Outline each Plasmodium malariae-infected red blood cell.
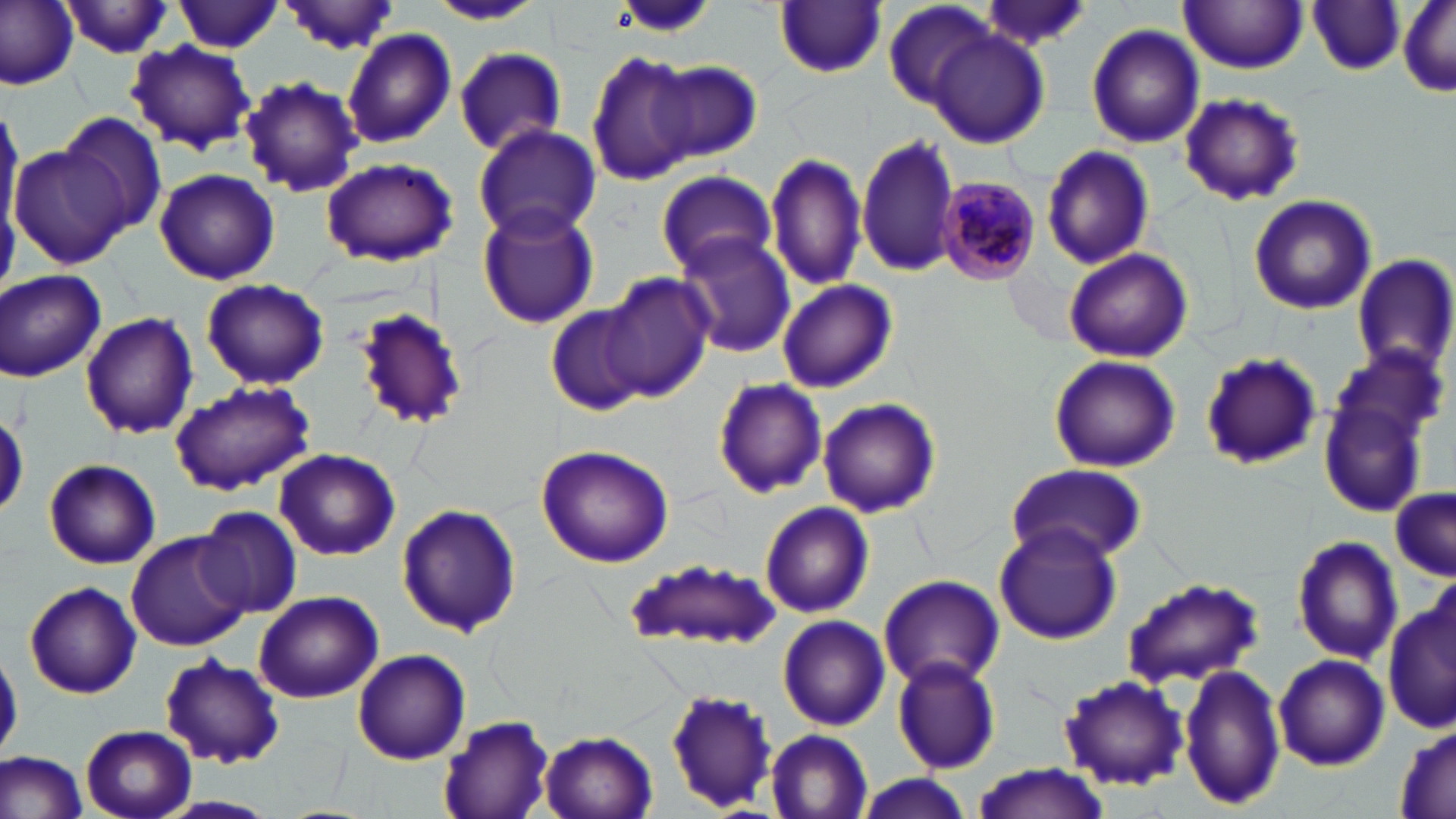
Approximate bounding boxes as (x1, y1, x2, y2) in pixels.
Plasmodium malariae-infected red blood cells: (942, 175, 1042, 283).

{
  "slide_level_diagnosis": "Plasmodium malariae",
  "magnification": "1000x",
  "stain": "May-Grünwald-Giemsa",
  "modality": "light microscopy",
  "image_size": "1456×819 pixels",
  "preparation": "thin blood film",
  "field_of_view": "single",
  "uninfected_red_blood_cell_locations": "approximate bounding boxes as (x1, y1, x2, y2) in pixels: (0, 0, 78, 90), (976, 0, 1094, 51), (175, 1, 284, 53), (426, 1, 547, 26), (881, 1, 996, 111), (277, 2, 404, 53), (1179, 2, 1309, 72), (1307, 2, 1406, 76), (1398, 2, 1455, 98), (61, 3, 179, 57), (775, 3, 886, 78), (1086, 23, 1205, 149), (341, 28, 456, 151), (928, 28, 1050, 146), (124, 41, 257, 155), (453, 46, 566, 157), (587, 50, 697, 186), (650, 59, 760, 161), (239, 76, 362, 198), (1177, 92, 1306, 208), (0, 98, 23, 235), (60, 111, 171, 237), (473, 121, 600, 242), (857, 132, 962, 276), (10, 140, 128, 266), (1041, 143, 1156, 270), (766, 150, 864, 292), (321, 156, 459, 268), (154, 168, 283, 285), (655, 170, 777, 278), (1248, 194, 1378, 316), (476, 203, 598, 330), (675, 233, 796, 357), (1063, 247, 1194, 364), (1353, 253, 1456, 377), (1, 270, 106, 381), (599, 274, 714, 403), (200, 277, 330, 390), (777, 280, 896, 393), (545, 305, 651, 416), (351, 306, 473, 432), (81, 312, 198, 439), (1199, 352, 1322, 472), (1048, 353, 1180, 472), (712, 378, 829, 498), (169, 381, 315, 494), (1320, 396, 1431, 518), (817, 398, 941, 517), (535, 444, 676, 569), (274, 448, 402, 560), (43, 458, 162, 569), (1005, 466, 1143, 565), (1388, 488, 1456, 579), (759, 500, 874, 617), (396, 502, 521, 639), (194, 508, 301, 618), (994, 522, 1123, 646), (124, 532, 250, 652), (1291, 534, 1403, 666), (623, 559, 786, 653), (878, 573, 1005, 691), (1121, 576, 1264, 691), (22, 580, 142, 699), (1385, 587, 1455, 740), (253, 590, 385, 704), (777, 615, 889, 730), (351, 648, 472, 765), (1, 650, 23, 757), (158, 653, 286, 768), (1274, 653, 1390, 770), (891, 654, 1002, 773), (1180, 663, 1286, 811), (1058, 675, 1189, 790), (666, 691, 780, 812), (439, 712, 558, 818), (1394, 722, 1455, 818), (80, 725, 197, 819), (766, 730, 873, 817), (540, 732, 659, 818), (0, 750, 89, 819), (968, 764, 1112, 819), (855, 775, 978, 818), (159, 797, 277, 818)"
}